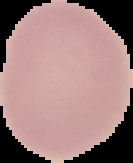
Cell region segmented out of the field of view; the surrounding area is masked to black. Image is 133×163 pixels. From a thin blood film. Malaria status: uninfected.